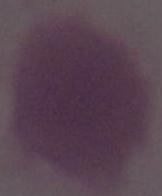
Summary:
  - Modality: photomicrograph
  - Identification: erythrocyte
  - Magnification: 1000x